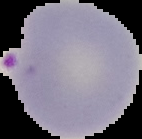 The area outside the segmented cell region is set to black. From a thin blood film. Image is 142×139 pixels. Result: malaria parasites detected.